Comment on the morphology of the erythrocytes.
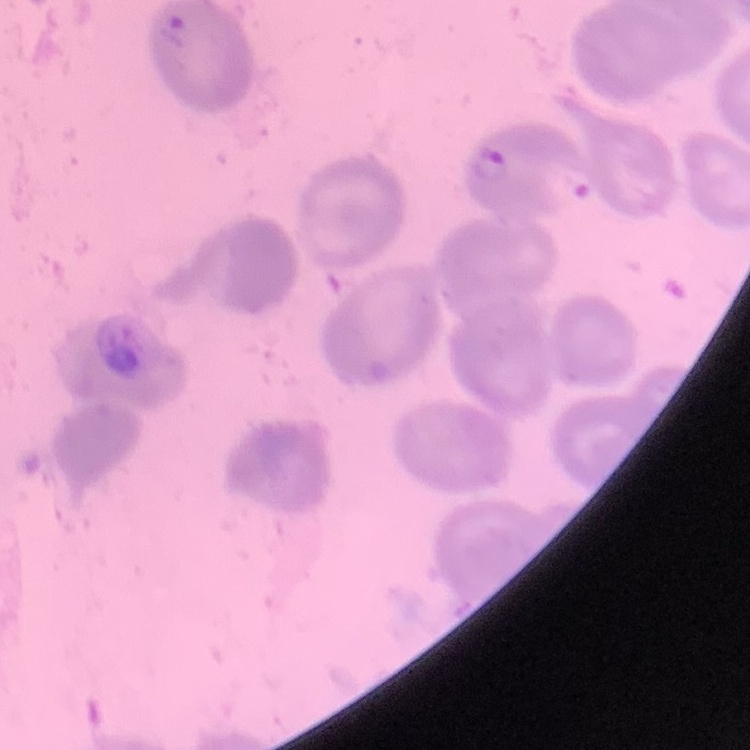

They show no rouleaux formation.

Square crop of a larger photomicrograph. Field's or Giemsa stain. Thin blood smear.